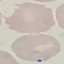

result: malaria parasites identified
image_type: cell patch, automatically extracted from a larger field of view and resized to 64 × 64 pixels
capture: smartphone camera at the microscope eyepiece
preparation: thin blood film
stain: Giemsa